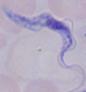

magnification = 1000x
modality = micrograph
identification = trypanosome